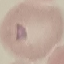

Summary:
  - Malaria status: uninfected
  - Image type: cell patch, automatically extracted from a larger field of view and resized to 64 × 64 pixels
  - Preparation: thin blood smear
  - Stain: Giemsa
  - Capture: smartphone camera at the microscope eyepiece